Locate every Plasmodium parasite.
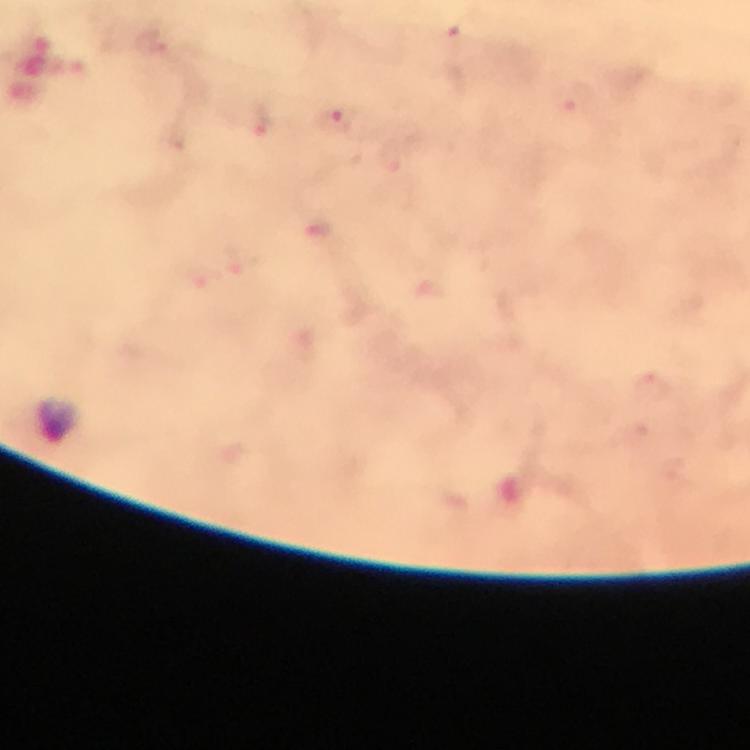
Approximate centers as [x, y] in pixels.
Plasmodium parasites: [155, 37], [334, 120], [260, 124], [389, 163].

Giemsa-stained preparation. Thick smear. Cropped region of a single field of view. From a diagnostic examination for malaria. 100x magnification. Immersion oil applied. Photographed through the microscope with a smartphone camera. Image is 750×750 pixels.